Identify the blood parasite species.
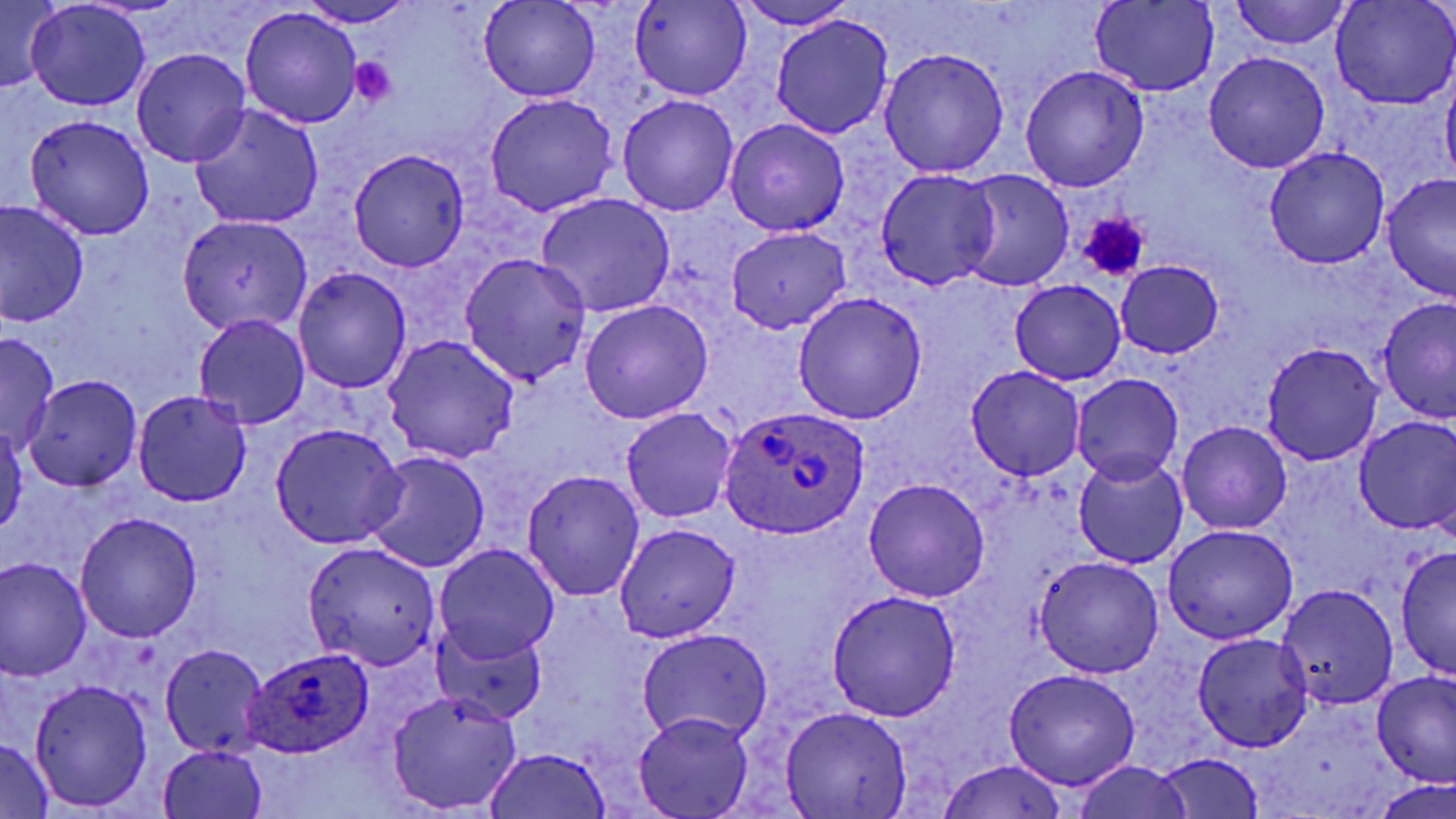
Plasmodium ovale.

{
  "field_of_view": "single",
  "preparation": "thin blood film",
  "platelet_locations": "approximate bounding boxes as (x1,y1)-(x2,y2) corner pairs in pixels: (350,57)-(397,106), (1077,213)-(1150,282)",
  "image_size": "1456×819 pixels",
  "uninfected_red_blood_cell_locations": "approximate bounding boxes as (x1,y1)-(x2,y2) corner pairs in pixels: (0,0)-(62,94), (631,0)-(751,101), (733,0)-(860,30), (1331,0)-(1455,108), (295,1)-(420,27), (479,1)-(599,102), (1230,1)-(1350,50), (25,2)-(149,111), (1089,2)-(1219,96), (240,9)-(361,128), (771,15)-(894,141), (879,46)-(1009,177), (132,49)-(251,167), (1204,51)-(1330,173), (1019,65)-(1150,192), (1441,73)-(1456,190), (483,93)-(619,217), (618,94)-(739,215), (191,104)-(324,229), (24,114)-(156,240), (726,118)-(849,236), (1264,146)-(1390,270), (349,150)-(469,272), (876,169)-(1000,290), (955,171)-(1075,292), (1381,174)-(1455,303), (536,193)-(675,317), (0,200)-(90,325), (179,216)-(312,335), (728,227)-(850,334), (458,253)-(591,386), (1116,261)-(1224,359), (292,267)-(412,394), (1009,280)-(1126,384), (792,291)-(927,425), (1378,299)-(1456,423), (579,300)-(713,424), (193,315)-(310,430), (0,332)-(60,453), (382,334)-(519,464), (1261,342)-(1383,465), (967,365)-(1086,481), (1072,373)-(1183,486), (24,376)-(142,491), (132,389)-(252,507), (621,406)-(737,523), (1354,415)-(1456,536), (0,420)-(25,540), (1177,421)-(1293,535), (269,422)-(408,549), (363,451)-(490,573), (1072,454)-(1189,570), (521,469)-(645,600), (863,477)-(992,602), (73,513)-(203,642), (615,523)-(739,642), (1162,524)-(1298,645), (302,541)-(441,670), (434,544)-(560,664), (1395,545)-(1455,682), (1034,557)-(1164,677), (0,558)-(92,681), (1277,584)-(1398,709), (826,590)-(961,721), (433,625)-(546,726), (636,628)-(775,746), (1192,633)-(1314,752), (160,643)-(268,759), (1003,668)-(1139,789), (1370,671)-(1456,789), (30,680)-(152,811), (387,689)-(524,814), (781,706)-(913,817), (633,713)-(753,819), (0,740)-(54,818), (158,744)-(269,819), (482,747)-(615,818), (1152,752)-(1265,818), (936,759)-(1070,819), (1070,761)-(1195,819), (1374,779)-(1456,818)",
  "stain": "May-Grünwald-Giemsa",
  "plasmodium_ovale_infected_red_blood_cell_locations": "approximate bounding boxes as (x1,y1)-(x2,y2) corner pairs in pixels: (715,405)-(872,537), (233,652)-(373,758)",
  "magnification": "1000x",
  "modality": "light microscopy"
}